Report the malaria status of this cell.
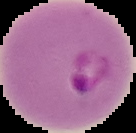

It is parasitized.

From a thin blood film. Cell region segmented out of the field of view; the surrounding area is masked to black. Image is 136×133 pixels.